Classify this cell by malaria status.
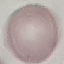
It is uninfected.

Giemsa stain. Thin blood film. Photographed with a smartphone camera at the microscope eyepiece. Cell patch, automatically extracted from a larger field of view and resized to 64 × 64 pixels.